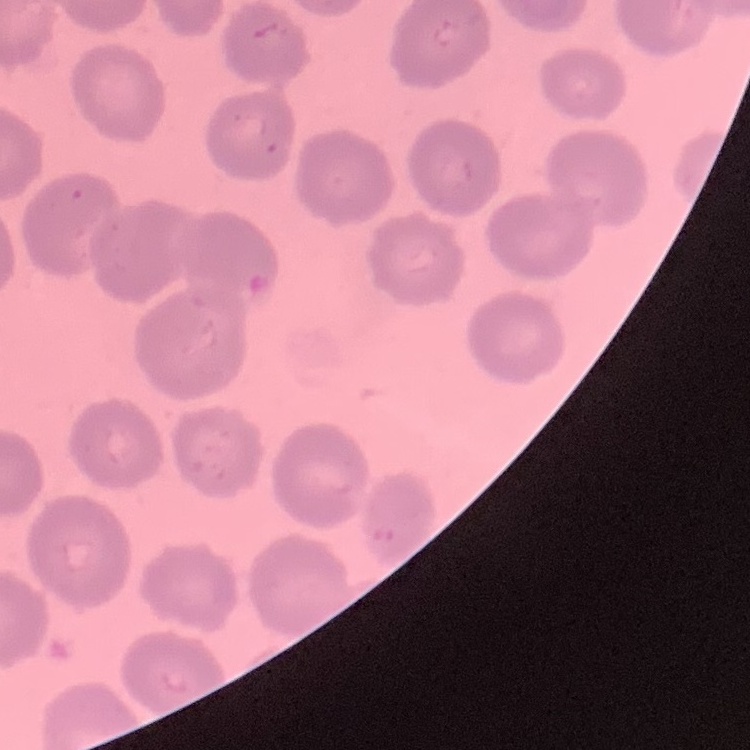

The red blood cells exhibit no rouleaux formation. Thin blood smear. Stained with either Field's or Giemsa. Square crop of a larger photomicrograph.